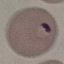

Summary:
  - Result: malaria parasites detected
  - Stain: Giemsa
  - Capture: smartphone through the microscope eyepiece
  - Image type: automatically extracted cell patch, resized to 64 × 64 pixels
  - Preparation: thin blood film